Assess this cell for malaria.
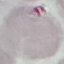
It is uninfected.

stain = Giemsa
preparation = thin smear
image type = automatically extracted cell patch, resized to 64 × 64 pixels
capture = smartphone through the microscope eyepiece